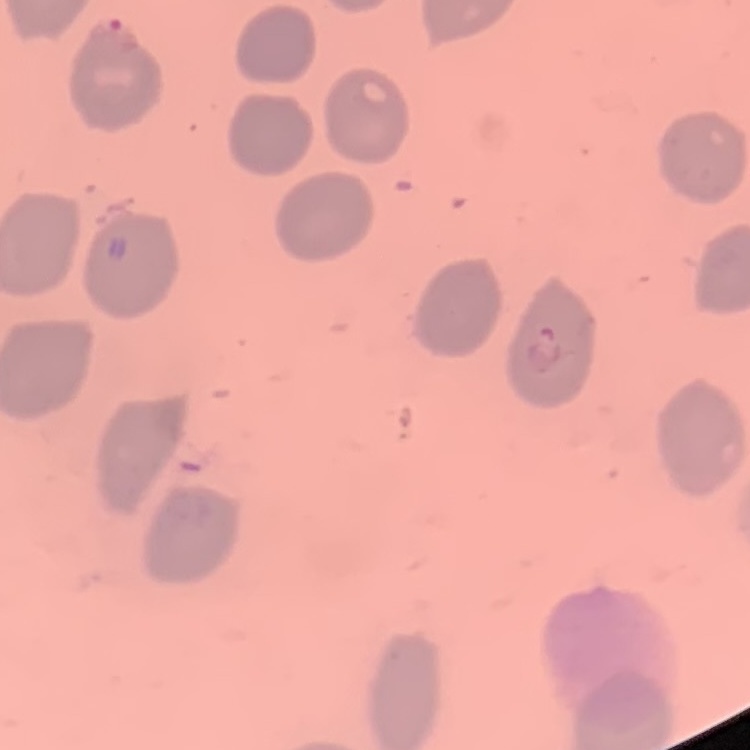
Summary:
  - Erythrocyte morphology: no rouleaux formation
  - Preparation: thin peripheral smear
  - Image type: one tile cut from a larger photomicrograph
  - Stain: Field's or Giemsa